Describe the morphology of the red blood cells.
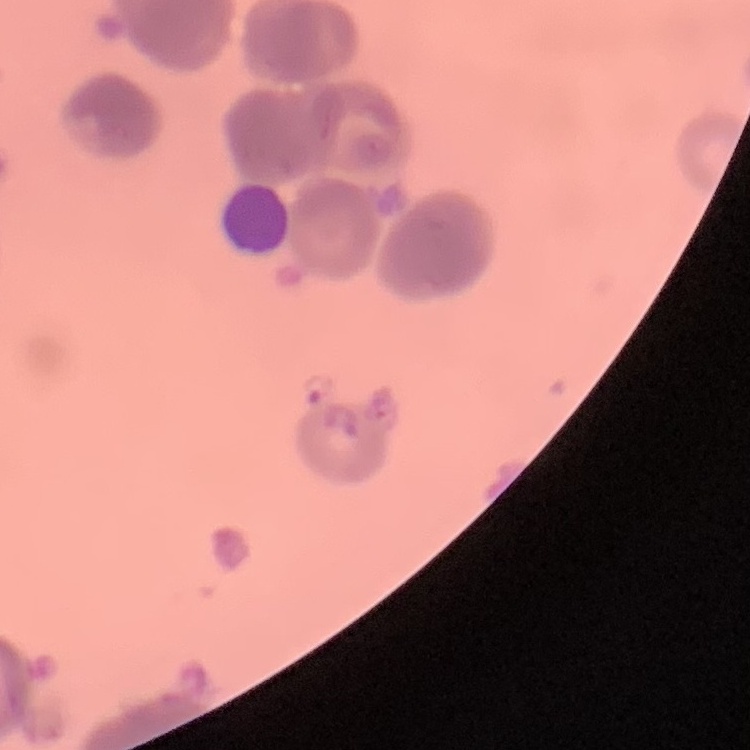

Rouleaux formation.

Summary:
  - Preparation: thin peripheral smear
  - Image type: one tile cut from a larger photomicrograph
  - Stain: Field's or Giemsa